Comment on the morphology of the red blood cells.
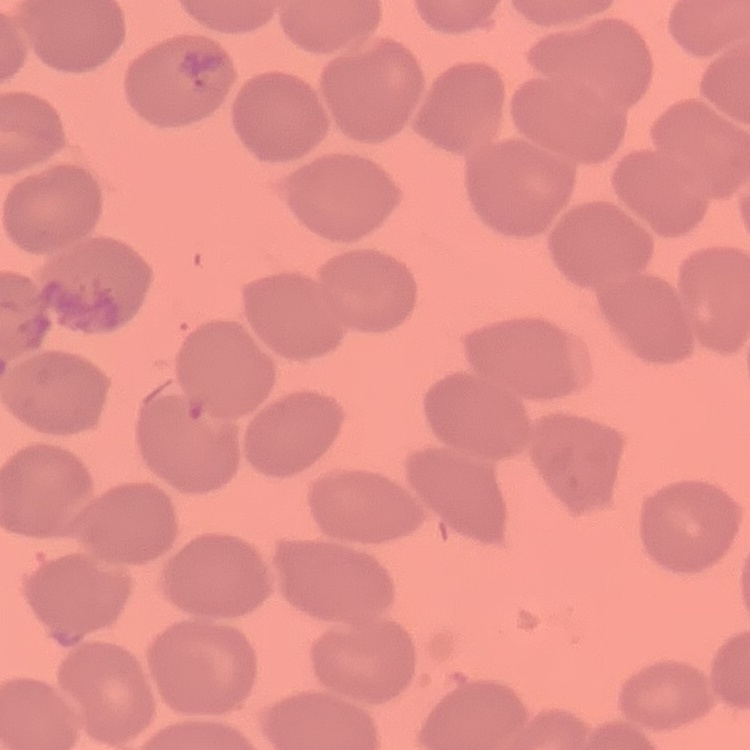
They show no rouleaux formation.

image type = one tile cut from a larger photomicrograph
stain = Field's or Giemsa
preparation = thin blood smear